Name the cell type shown.
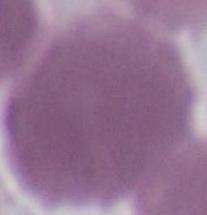

This is an erythrocyte.

Photomicrograph. 1000x magnification.